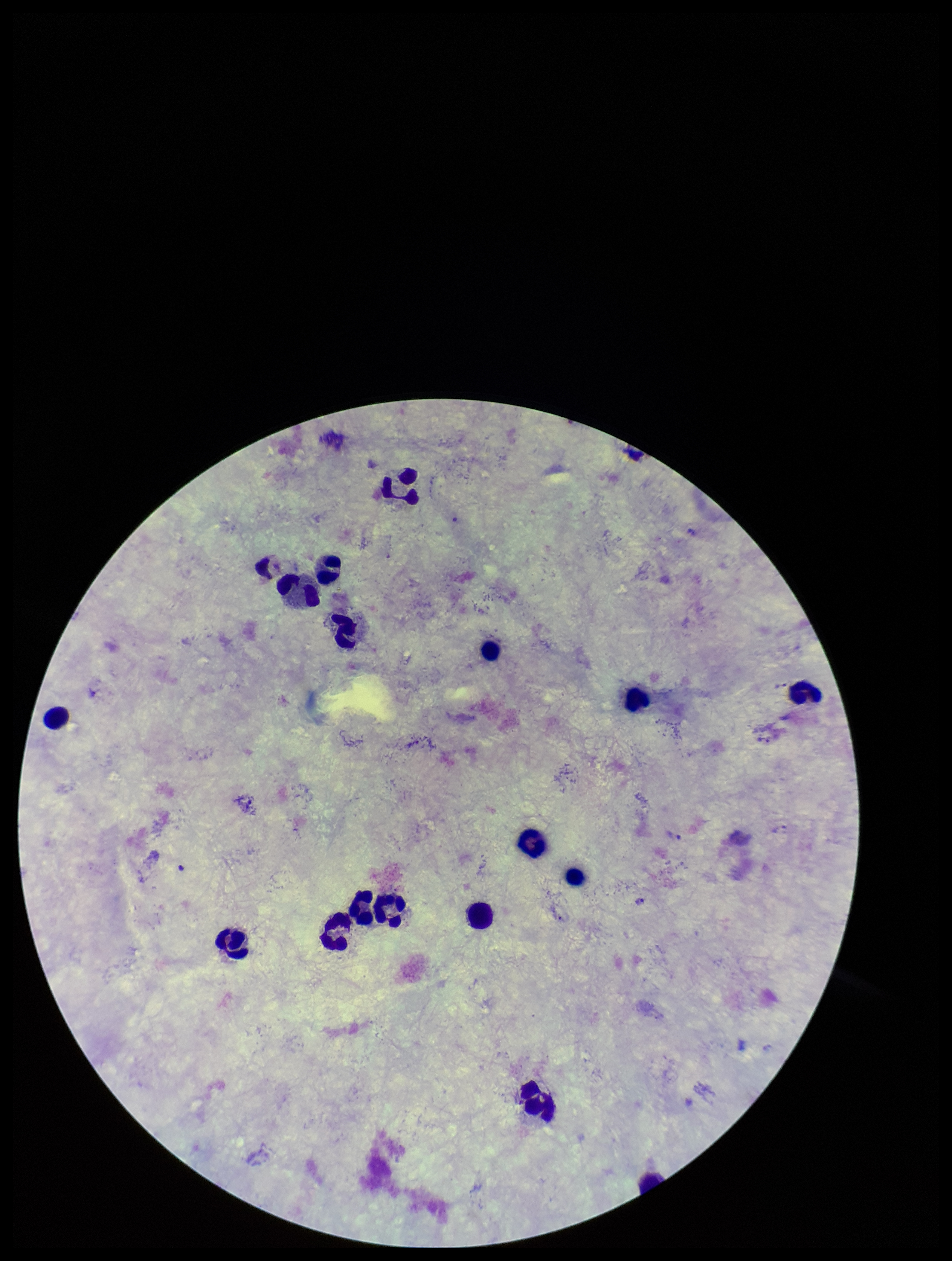

Summary:
  - Image size: 952×1261 pixels
  - Plasmodium parasites: none identified
  - Species reported for this patient: Plasmodium vivax
  - Patient malaria status: positive
  - Field of view: single
  - Parasite count: 0
  - Stain: Giemsa
  - Preparation: thick
  - Leukocyte count: 18
  - Capture: smartphone photograph through the microscope eyepiece